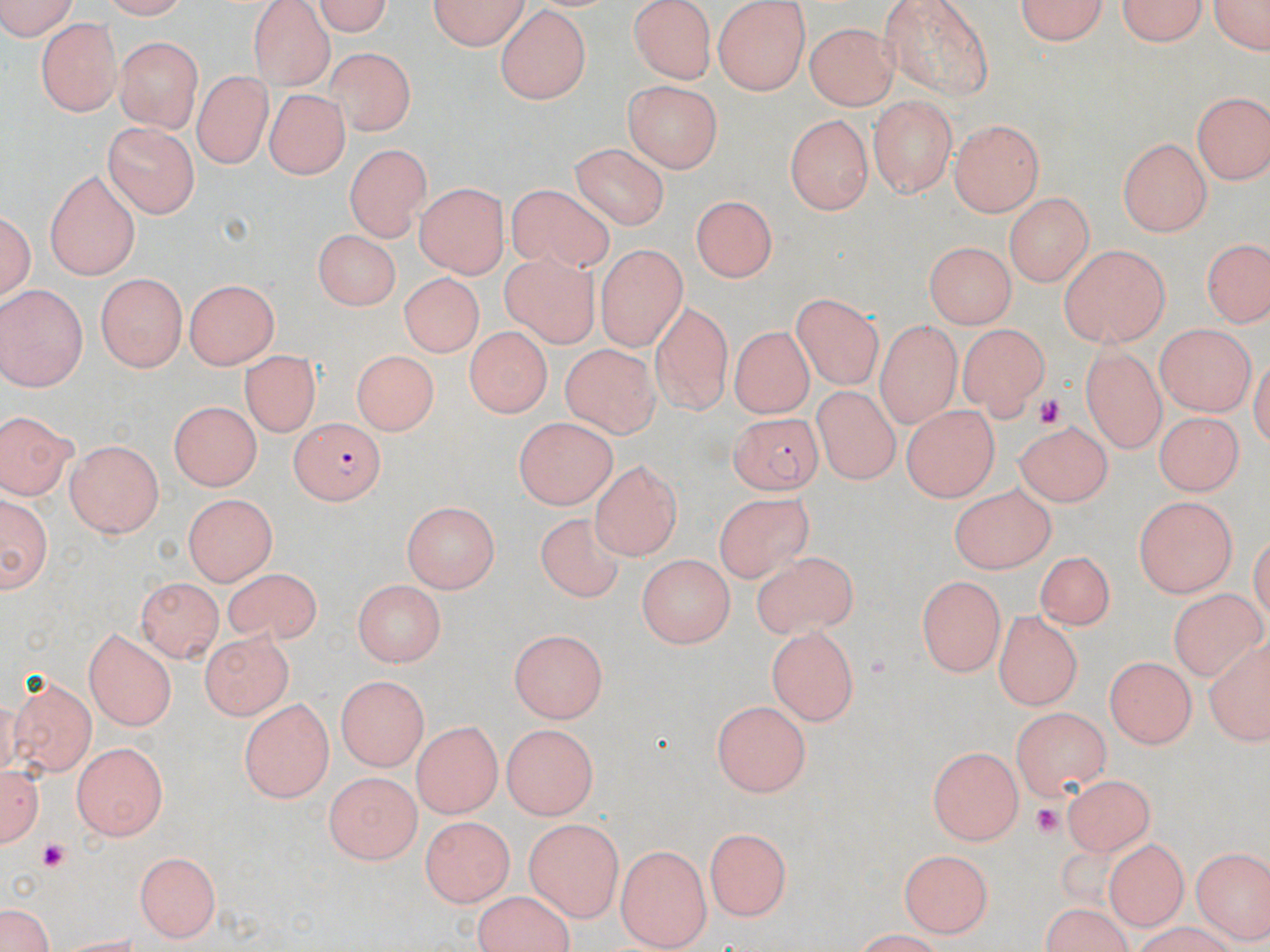
Summary:
  - Coordinate format: approximate bounding boxes as named x1/y1/x2/y2 corners in pixels
  - Platelet locations: (x1=1030, y1=396, x2=1063, y2=427), (x1=1027, y1=803, x2=1067, y2=840), (x1=36, y1=843, x2=68, y2=872)
  - Uninfected red blood cell locations: (x1=0, y1=0, x2=85, y2=38), (x1=306, y1=0, x2=399, y2=33), (x1=426, y1=0, x2=532, y2=49), (x1=628, y1=0, x2=719, y2=81), (x1=874, y1=0, x2=992, y2=97), (x1=1017, y1=0, x2=1112, y2=48), (x1=1115, y1=0, x2=1209, y2=49), (x1=1204, y1=0, x2=1270, y2=61), (x1=249, y1=1, x2=338, y2=90), (x1=711, y1=1, x2=815, y2=96), (x1=494, y1=7, x2=591, y2=105), (x1=38, y1=18, x2=120, y2=114), (x1=803, y1=24, x2=897, y2=109), (x1=114, y1=36, x2=204, y2=131), (x1=326, y1=44, x2=417, y2=132), (x1=193, y1=72, x2=270, y2=169), (x1=622, y1=80, x2=723, y2=175), (x1=268, y1=87, x2=346, y2=181), (x1=1191, y1=90, x2=1268, y2=186), (x1=868, y1=96, x2=955, y2=195), (x1=785, y1=112, x2=875, y2=214), (x1=950, y1=120, x2=1041, y2=216), (x1=104, y1=123, x2=197, y2=220), (x1=1118, y1=135, x2=1212, y2=236), (x1=571, y1=143, x2=673, y2=230), (x1=343, y1=145, x2=430, y2=243), (x1=42, y1=170, x2=142, y2=279), (x1=417, y1=182, x2=506, y2=281), (x1=505, y1=187, x2=617, y2=272), (x1=1005, y1=193, x2=1093, y2=288), (x1=690, y1=196, x2=776, y2=283), (x1=2, y1=201, x2=37, y2=309), (x1=310, y1=231, x2=401, y2=311), (x1=1204, y1=237, x2=1266, y2=326), (x1=926, y1=239, x2=1016, y2=325), (x1=498, y1=244, x2=605, y2=352), (x1=596, y1=246, x2=685, y2=353), (x1=1058, y1=246, x2=1170, y2=346), (x1=402, y1=270, x2=483, y2=359), (x1=96, y1=274, x2=187, y2=372), (x1=185, y1=278, x2=279, y2=372), (x1=0, y1=285, x2=89, y2=389), (x1=785, y1=292, x2=884, y2=382), (x1=651, y1=299, x2=733, y2=416), (x1=874, y1=320, x2=967, y2=434), (x1=957, y1=323, x2=1049, y2=421), (x1=1154, y1=323, x2=1255, y2=417), (x1=728, y1=324, x2=813, y2=418), (x1=462, y1=327, x2=551, y2=415), (x1=558, y1=342, x2=657, y2=440), (x1=1080, y1=346, x2=1165, y2=451), (x1=352, y1=350, x2=434, y2=435), (x1=242, y1=352, x2=318, y2=440), (x1=810, y1=385, x2=906, y2=482), (x1=166, y1=400, x2=262, y2=489), (x1=897, y1=401, x2=995, y2=499), (x1=1154, y1=404, x2=1236, y2=497), (x1=0, y1=412, x2=73, y2=503), (x1=512, y1=417, x2=618, y2=507), (x1=1013, y1=418, x2=1117, y2=508), (x1=65, y1=440, x2=166, y2=538), (x1=589, y1=462, x2=687, y2=562), (x1=946, y1=483, x2=1057, y2=572), (x1=1, y1=491, x2=52, y2=596), (x1=698, y1=491, x2=818, y2=586), (x1=182, y1=493, x2=279, y2=586), (x1=1134, y1=496, x2=1235, y2=597), (x1=401, y1=501, x2=496, y2=591), (x1=532, y1=511, x2=625, y2=602), (x1=744, y1=547, x2=861, y2=641), (x1=1033, y1=550, x2=1120, y2=629), (x1=638, y1=552, x2=737, y2=646), (x1=212, y1=573, x2=329, y2=646), (x1=916, y1=576, x2=1002, y2=677), (x1=136, y1=577, x2=224, y2=660), (x1=355, y1=580, x2=448, y2=665), (x1=1164, y1=584, x2=1265, y2=682), (x1=994, y1=609, x2=1082, y2=709), (x1=766, y1=625, x2=857, y2=727), (x1=198, y1=628, x2=286, y2=718), (x1=510, y1=629, x2=609, y2=721), (x1=81, y1=630, x2=176, y2=730), (x1=1210, y1=636, x2=1270, y2=747), (x1=1105, y1=657, x2=1194, y2=750), (x1=9, y1=675, x2=97, y2=774), (x1=334, y1=675, x2=430, y2=771), (x1=238, y1=698, x2=333, y2=803), (x1=710, y1=699, x2=811, y2=797), (x1=1010, y1=707, x2=1113, y2=802), (x1=415, y1=722, x2=499, y2=818), (x1=502, y1=723, x2=595, y2=820), (x1=72, y1=739, x2=166, y2=840), (x1=928, y1=743, x2=1025, y2=843), (x1=2, y1=762, x2=44, y2=850), (x1=324, y1=770, x2=423, y2=860), (x1=1062, y1=773, x2=1155, y2=855), (x1=412, y1=815, x2=508, y2=916), (x1=523, y1=820, x2=626, y2=919), (x1=706, y1=827, x2=793, y2=922), (x1=1106, y1=837, x2=1191, y2=930), (x1=617, y1=846, x2=712, y2=946), (x1=1191, y1=846, x2=1269, y2=942), (x1=897, y1=847, x2=991, y2=936), (x1=137, y1=851, x2=222, y2=937), (x1=2, y1=908, x2=52, y2=952), (x1=1120, y1=924, x2=1243, y2=952)
  - Plasmodium falciparum-infected red blood cell locations: (x1=732, y1=415, x2=824, y2=495), (x1=288, y1=417, x2=387, y2=502)
  - Slide-level diagnosis: Plasmodium falciparum
  - Modality: optical microscopy
  - Stain: May-Grünwald-Giemsa
  - Magnification: 1000x
  - Preparation: thin blood film
  - Field of view: one of a larger specimen
  - Image size: 1270×952 pixels